Classify this cell by malaria status.
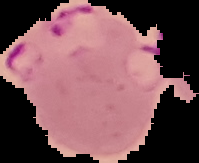

It is parasitized.

image size = 199×163 pixels
preparation = thin blood smear
image type = cell region segmented out of the field of view; surrounding area masked to black